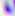

Summary:
  - Identification: Toxoplasma gondii
  - Modality: micrograph
  - Magnification: 400x